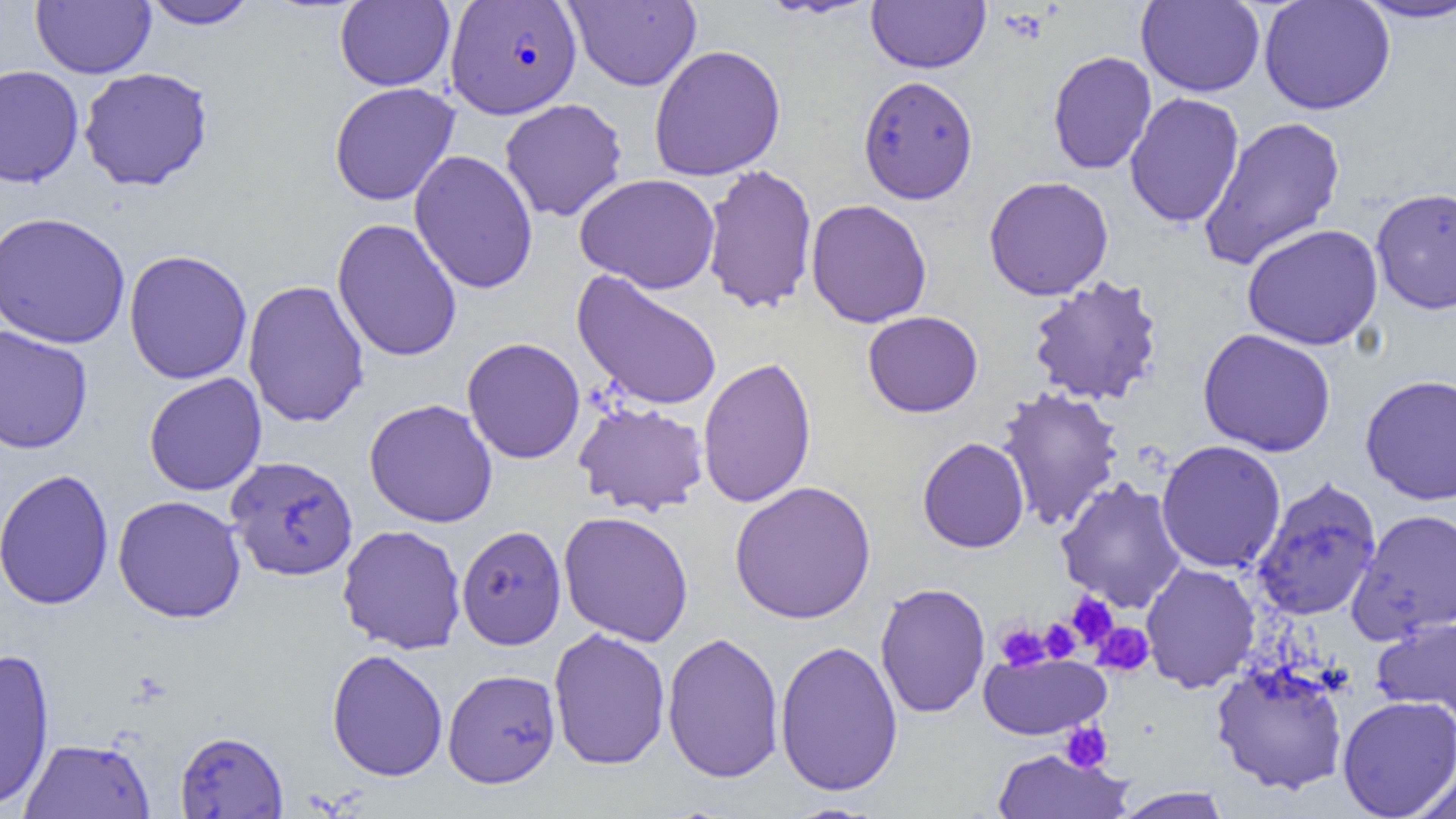

Summary:
  - Coordinate format: approximate bounding boxes as (x1, y1, x2, y2) in pixels
  - Plasmodium falciparum-infected red blood cell locations: (446, 1, 581, 118)
  - Platelet locations: (1066, 592, 1119, 649), (1038, 619, 1081, 663), (1092, 622, 1154, 676), (995, 623, 1050, 671), (1059, 721, 1113, 773)
  - Uninfected red blood cell locations: (32, 0, 155, 78), (142, 0, 259, 29), (565, 0, 702, 92), (1259, 0, 1395, 115), (335, 1, 455, 91), (867, 1, 990, 73), (1136, 1, 1265, 97), (1353, 1, 1456, 23), (648, 44, 786, 181), (1048, 50, 1157, 174), (0, 64, 84, 188), (78, 67, 214, 191), (858, 75, 979, 204), (329, 82, 460, 206), (1124, 93, 1245, 228), (499, 98, 628, 222), (1198, 114, 1346, 271), (409, 149, 539, 295), (701, 164, 818, 314), (575, 173, 721, 294), (983, 175, 1114, 300), (1370, 187, 1456, 314), (805, 199, 932, 328), (0, 211, 131, 349), (332, 218, 462, 362), (1242, 223, 1384, 350), (123, 249, 253, 385), (571, 270, 723, 411), (1026, 275, 1164, 406), (242, 279, 369, 428), (862, 311, 984, 417), (0, 324, 93, 454), (1197, 328, 1336, 457), (462, 337, 586, 464), (697, 356, 817, 509), (144, 372, 267, 496), (1360, 373, 1456, 506), (995, 387, 1124, 532), (364, 398, 498, 528), (573, 400, 709, 516), (917, 436, 1030, 553), (1156, 440, 1287, 574), (226, 456, 358, 581), (0, 468, 115, 610), (1251, 476, 1382, 622), (1055, 477, 1187, 612), (729, 480, 877, 624), (113, 495, 246, 623), (1347, 508, 1456, 643), (557, 510, 694, 647), (337, 524, 467, 654), (456, 524, 567, 650), (1140, 561, 1261, 693), (875, 582, 990, 718), (1373, 617, 1456, 722), (548, 627, 671, 771), (662, 631, 785, 783), (774, 640, 904, 796), (0, 647, 56, 810), (326, 649, 448, 782), (979, 653, 1111, 740), (1210, 660, 1349, 794), (443, 668, 561, 788), (1337, 695, 1456, 818), (175, 730, 288, 818), (20, 738, 155, 819), (992, 748, 1132, 818), (1410, 761, 1456, 819), (1112, 786, 1234, 818), (779, 802, 888, 819)
  - Slide-level diagnosis: Plasmodium falciparum
  - Preparation: thin blood film
  - Magnification: 1000x
  - Field of view: single
  - Modality: light microscopy
  - Image size: 1456×819 pixels